State which parasite is depicted.
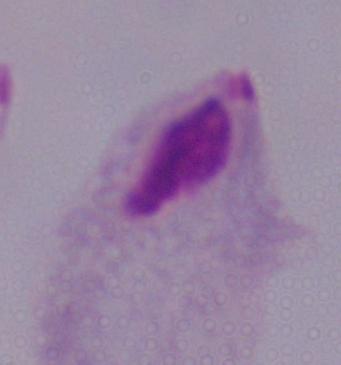
This is a trichomonad.

Micrograph. 1000x magnification.